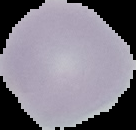
Summary:
  - Image type: cell region segmented out of the field of view; surrounding area masked to black
  - Image size: 136×130 pixels
  - Result: negative for Plasmodium parasites
  - Preparation: thin blood film